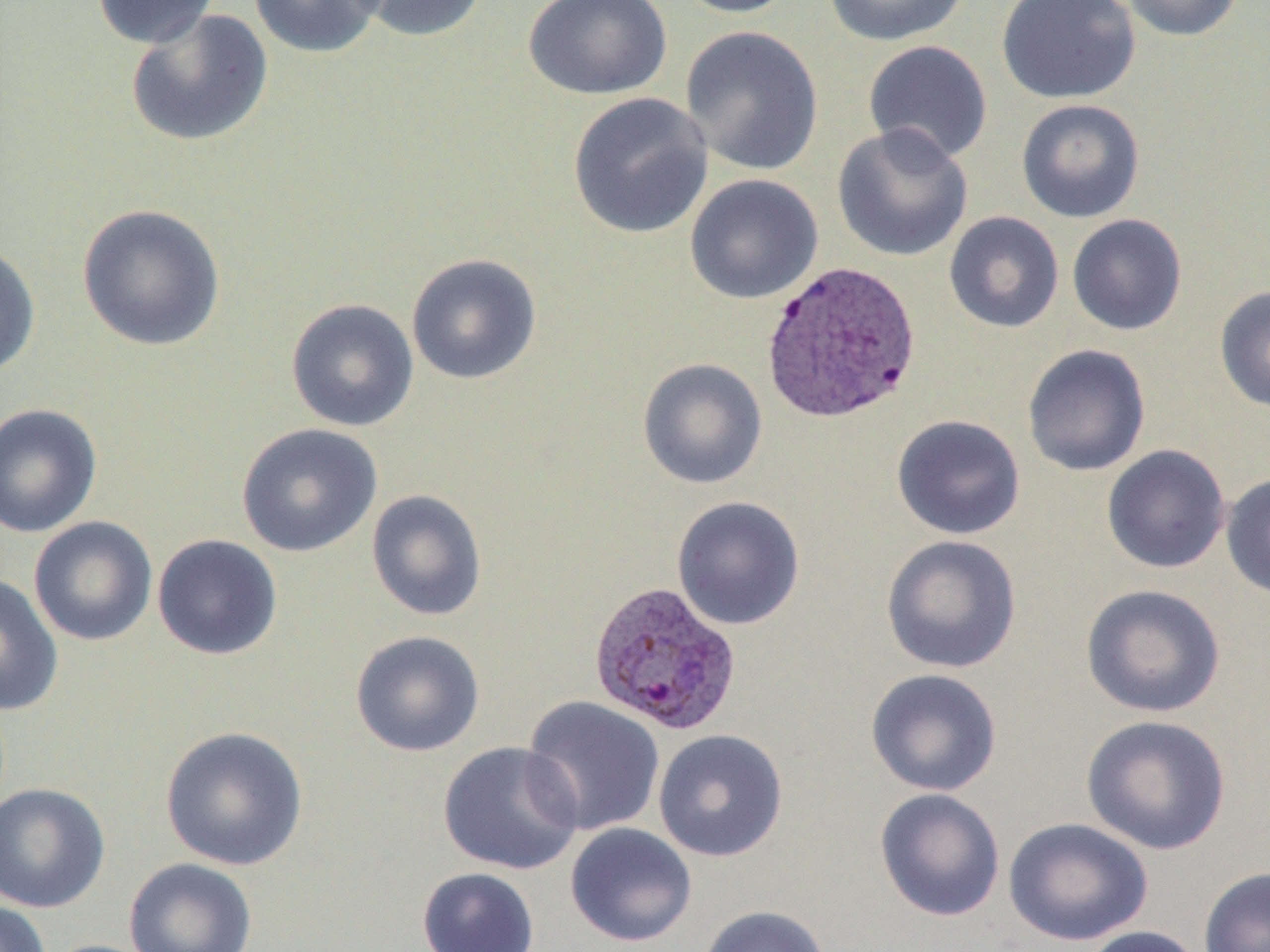
Approximate bounding boxes as [x1, y1, x2, y2] in pixels. Uninfected red blood cell locations: [92, 0, 221, 49], [249, 0, 386, 58], [350, 0, 489, 43], [522, 0, 673, 100], [669, 0, 800, 18], [820, 0, 972, 47], [996, 0, 1141, 105], [1117, 0, 1246, 42], [125, 9, 273, 148], [679, 25, 824, 176], [862, 40, 993, 165], [567, 92, 714, 239], [1016, 98, 1146, 222], [831, 124, 974, 263], [684, 173, 823, 305], [76, 203, 226, 352], [943, 211, 1064, 333], [1066, 214, 1187, 336], [0, 243, 41, 380], [406, 253, 542, 385], [1214, 285, 1270, 413], [285, 298, 420, 432], [1021, 343, 1151, 477], [636, 358, 768, 490], [0, 403, 102, 539], [891, 414, 1026, 540], [236, 423, 383, 557], [1101, 444, 1231, 574], [1221, 472, 1270, 600], [366, 489, 488, 622], [671, 496, 806, 631], [28, 516, 158, 646], [152, 533, 283, 660], [881, 534, 1022, 674], [0, 573, 63, 716], [1080, 583, 1226, 718], [349, 630, 485, 757], [865, 668, 1002, 797], [521, 695, 665, 836], [1080, 714, 1232, 855], [160, 725, 309, 871], [653, 729, 788, 862], [438, 740, 584, 875], [0, 782, 111, 913], [874, 787, 1006, 921], [1003, 817, 1153, 946], [565, 822, 697, 947], [123, 857, 258, 952], [416, 866, 540, 952], [1199, 866, 1270, 952], [0, 900, 51, 952], [699, 904, 831, 952], [1080, 925, 1205, 952], [38, 939, 163, 952]. Plasmodium vivax-infected red blood cell locations: [760, 259, 922, 424], [587, 579, 743, 736]. Slide-level diagnosis: Plasmodium vivax. Image is 1270×952 pixels. Optical microscopy. One field of a larger specimen. Captured at 1000x magnification. Thin blood film.